State which parasite is depicted.
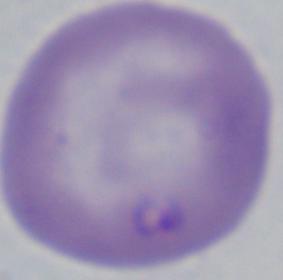
Babesia.

Micrograph. 1000x magnification.